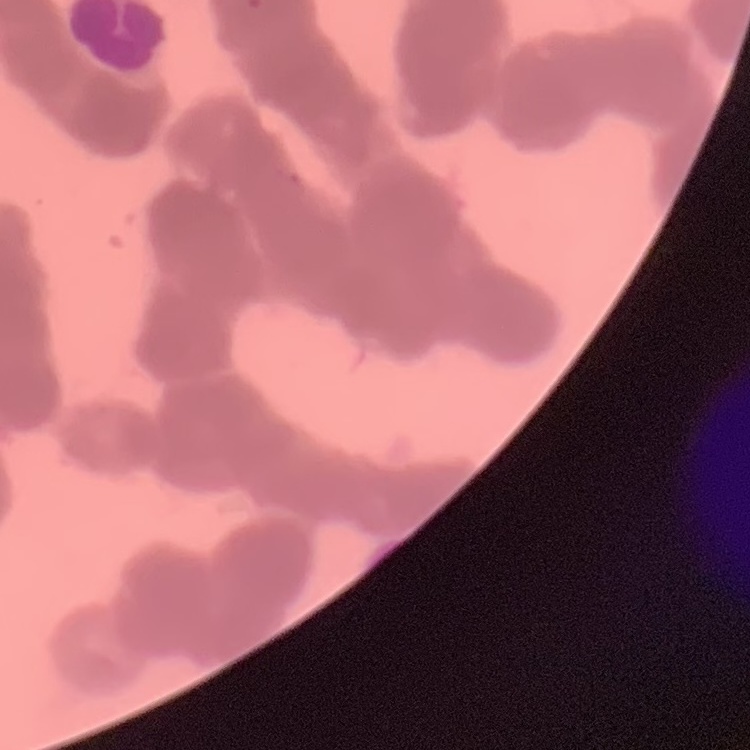
Summary:
  - Erythrocyte morphology: rouleaux formation
  - Image type: square crop of a larger photomicrograph
  - Preparation: thin peripheral smear
  - Stain: Field's or Giemsa